State the blood parasite species.
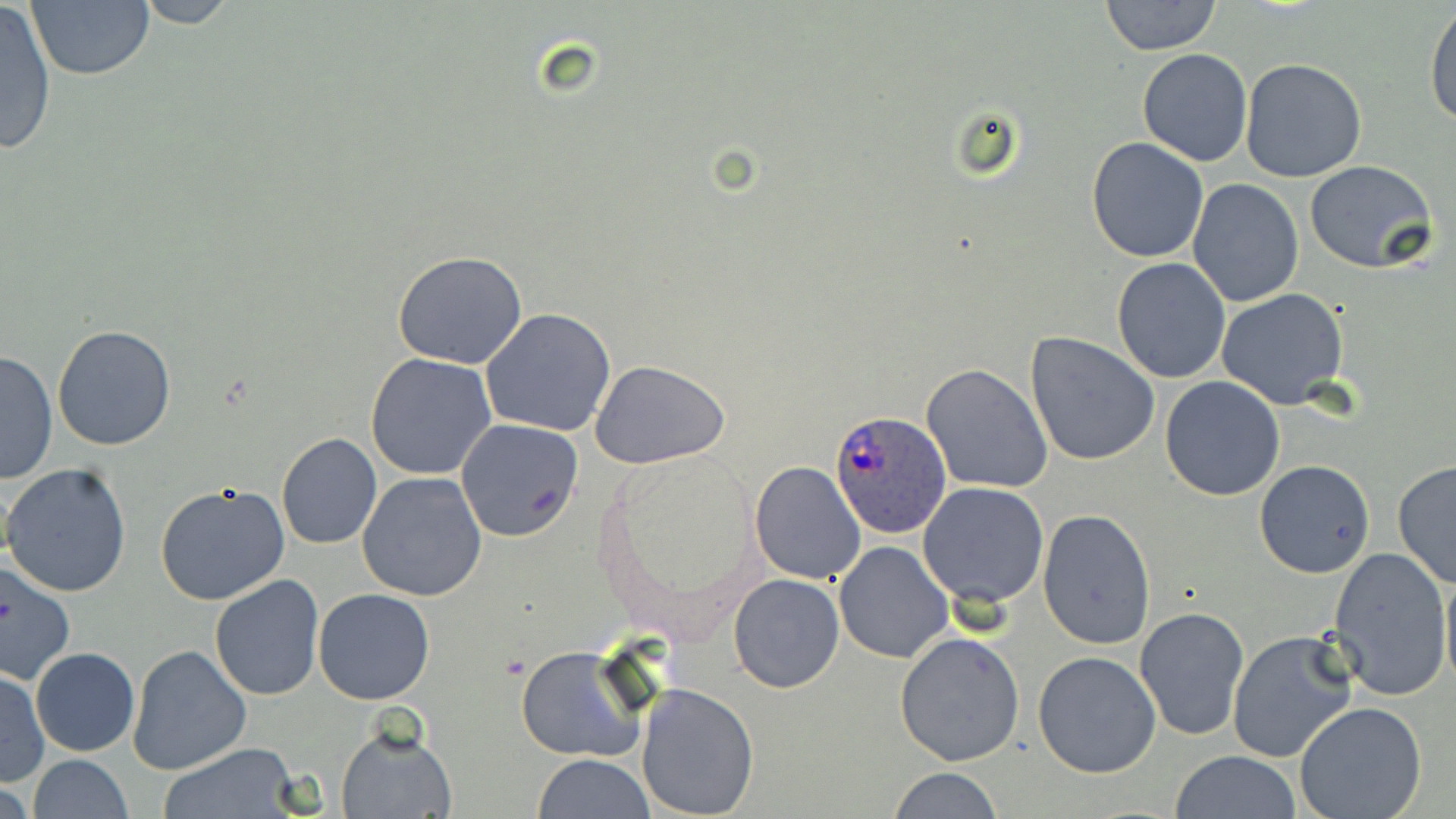

Plasmodium ovale.

Approximate bounding boxes as named x1/y1/x2/y2 corners in pixels. Plasmodium ovale-infected red blood cell locations: (x1=831, y1=411, x2=952, y2=538). Uninfected red blood cell locations: (x1=128, y1=0, x2=247, y2=28), (x1=1102, y1=0, x2=1221, y2=54), (x1=24, y1=1, x2=153, y2=82), (x1=0, y1=3, x2=58, y2=157), (x1=1425, y1=5, x2=1456, y2=128), (x1=1138, y1=48, x2=1252, y2=167), (x1=1240, y1=59, x2=1368, y2=183), (x1=1086, y1=136, x2=1211, y2=262), (x1=1304, y1=160, x2=1438, y2=274), (x1=1187, y1=179, x2=1303, y2=306), (x1=392, y1=252, x2=529, y2=369), (x1=1112, y1=258, x2=1232, y2=385), (x1=1214, y1=289, x2=1350, y2=410), (x1=479, y1=309, x2=617, y2=436), (x1=53, y1=324, x2=177, y2=450), (x1=1025, y1=332, x2=1160, y2=467), (x1=0, y1=350, x2=56, y2=486), (x1=366, y1=353, x2=497, y2=480), (x1=591, y1=360, x2=732, y2=469), (x1=921, y1=364, x2=1052, y2=493), (x1=1160, y1=375, x2=1286, y2=501), (x1=454, y1=418, x2=584, y2=542), (x1=277, y1=433, x2=383, y2=549), (x1=1254, y1=459, x2=1375, y2=577), (x1=750, y1=461, x2=867, y2=585), (x1=1392, y1=461, x2=1456, y2=588), (x1=1, y1=463, x2=132, y2=598), (x1=357, y1=472, x2=488, y2=602), (x1=918, y1=481, x2=1050, y2=608), (x1=155, y1=483, x2=291, y2=607), (x1=1038, y1=507, x2=1156, y2=652), (x1=833, y1=540, x2=955, y2=664), (x1=1328, y1=545, x2=1452, y2=703), (x1=1440, y1=557, x2=1456, y2=698), (x1=0, y1=558, x2=76, y2=685), (x1=729, y1=574, x2=844, y2=693), (x1=209, y1=576, x2=324, y2=701), (x1=313, y1=588, x2=435, y2=705), (x1=1134, y1=607, x2=1249, y2=739), (x1=1228, y1=629, x2=1358, y2=763), (x1=894, y1=631, x2=1025, y2=765), (x1=127, y1=645, x2=251, y2=773), (x1=517, y1=645, x2=646, y2=763), (x1=30, y1=647, x2=140, y2=756), (x1=1033, y1=650, x2=1162, y2=778), (x1=0, y1=662, x2=108, y2=779), (x1=0, y1=668, x2=50, y2=788), (x1=637, y1=683, x2=759, y2=817), (x1=1295, y1=701, x2=1428, y2=819), (x1=336, y1=726, x2=457, y2=819), (x1=158, y1=744, x2=302, y2=819), (x1=1170, y1=751, x2=1301, y2=819), (x1=533, y1=754, x2=655, y2=818), (x1=26, y1=756, x2=134, y2=818), (x1=889, y1=766, x2=1003, y2=819). Thin blood smear. One field of a larger specimen. Light microscopy. Captured at 1000x magnification. May-Grünwald-Giemsa stain. Image is 1456×819 pixels.